Locate every malaria parasite and every leukocyte.
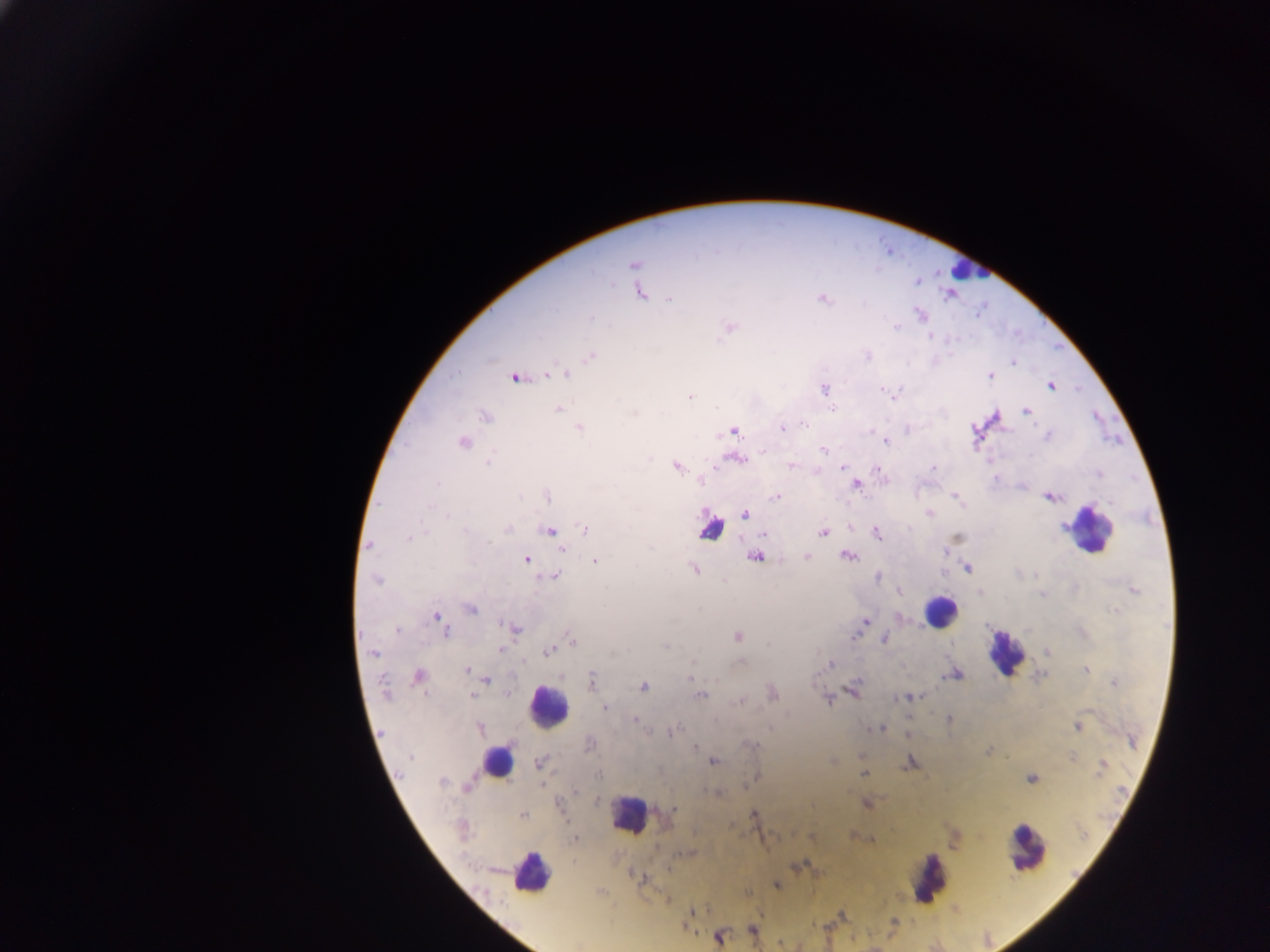
Approximate centers as {x, y} in pixels.
Malaria parasites: {634, 264}, {640, 293}, {669, 299}, {822, 299}, {920, 314}, {896, 326}, {730, 327}, {930, 335}, {591, 356}, {867, 356}, {1014, 362}, {556, 373}, {565, 374}, {990, 376}, {516, 378}, {1051, 385}, {823, 390}, {887, 391}, {895, 392}, {690, 397}, {832, 408}, {558, 410}, {1026, 411}, {634, 413}, {485, 417}, {804, 424}, {579, 428}, {783, 428}, {733, 431}, {1048, 436}, {886, 441}, {463, 443}, {823, 450}, {764, 452}, {737, 459}, {489, 462}, {676, 466}, {791, 466}, {843, 468}, {933, 468}, {1100, 475}, {702, 481}, {437, 483}, {856, 485}, {547, 496}, {957, 496}, {775, 498}, {1049, 498}, {1110, 502}, {744, 514}, {928, 514}, {447, 515}, {1064, 526}, {585, 529}, {466, 530}, {507, 530}, {550, 530}, {823, 533}, {877, 533}, {764, 534}, {956, 537}, {409, 538}, {369, 546}, {561, 549}, {945, 552}, {807, 556}, {848, 556}, {756, 557}, {526, 559}, {595, 561}, {967, 569}, {694, 570}, {554, 576}, {877, 578}, {377, 580}, {1133, 590}, {900, 592}, {980, 592}, {1043, 594}, {470, 609}, {1114, 611}, {435, 617}, {865, 621}, {513, 628}, {398, 630}, {446, 632}, {855, 635}, {737, 636}, {884, 639}, {572, 640}, {666, 647}, {501, 650}, {549, 651}, {1047, 652}, {374, 653}, {741, 662}, {831, 663}, {1085, 669}, {468, 670}, {953, 675}, {418, 676}, {690, 678}, {487, 679}, {592, 679}, {1114, 683}, {643, 686}, {385, 689}, {853, 690}, {772, 693}, {700, 695}, {472, 696}, {911, 697}, {902, 698}, {828, 700}, {738, 701}, {604, 707}, {949, 719}, {635, 720}, {1077, 727}, {479, 728}, {879, 729}, {672, 731}, {907, 734}, {1132, 741}, {589, 744}, {752, 745}, {694, 747}, {987, 751}, {411, 757}, {1073, 757}, {832, 761}, {713, 762}, {540, 763}, {909, 763}, {1102, 765}, {863, 774}, {598, 775}, {757, 777}, {1031, 780}, {442, 781}, {468, 785}, {576, 791}, {716, 792}, {598, 800}, {866, 804}, {560, 805}, {674, 809}, {754, 815}, {523, 816}, {462, 828}, {575, 838}, {871, 839}, {641, 878}, {776, 885}, {691, 913}, {893, 921}, {752, 929}, {719, 938}.
Leukocytes (some below the resolvable threshold): {964, 269}, {710, 532}, {1091, 533}, {940, 612}, {1004, 653}, {547, 707}, {497, 761}, {629, 815}, {1027, 850}, {530, 873}, {930, 878}.

Summary:
  - Country: Ghana
  - Field of view: single
  - Capture: mobile-phone photograph through a microscope
  - Image size: 1270×952 pixels
  - Preparation: thick blood smear